State the blood parasite species.
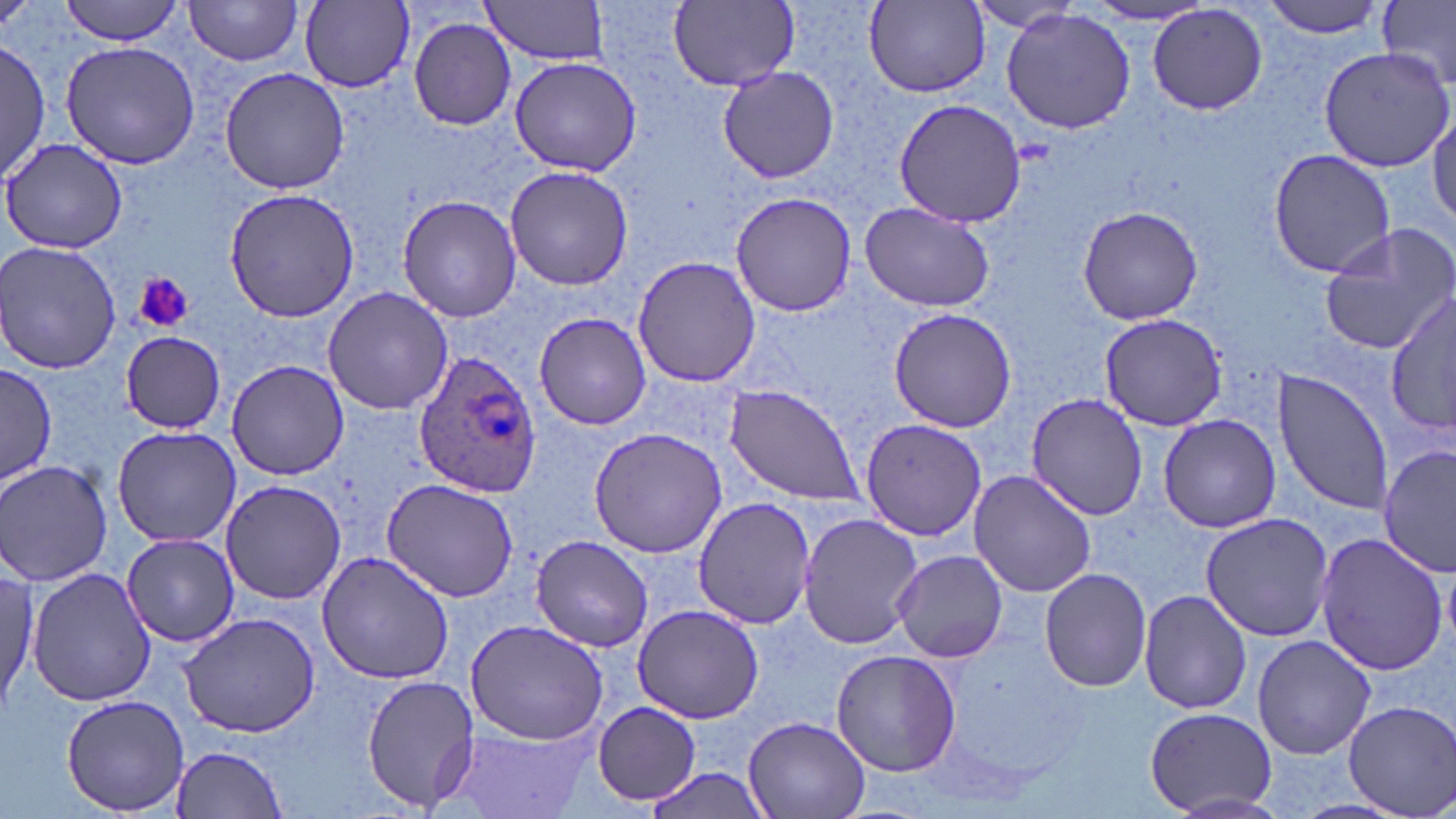

Plasmodium ovale.

Approximate bounding boxes as (x1,y1)-(x2,y2) corner pairs in pixels. Platelet locations: (136,273)-(194,333). Uninfected red blood cell locations: (62,0)-(187,45), (184,0)-(306,67), (300,0)-(417,91), (478,0)-(613,65), (1260,0)-(1392,39), (669,1)-(798,89), (865,1)-(991,97), (968,2)-(1089,33), (1377,2)-(1456,84), (1077,4)-(1212,26), (1147,4)-(1268,117), (1000,9)-(1138,135), (407,15)-(517,130), (0,39)-(50,181), (61,41)-(200,170), (1317,45)-(1456,172), (508,56)-(641,176), (219,66)-(349,194), (717,68)-(839,183), (892,98)-(1028,228), (1429,110)-(1455,226), (1,138)-(129,256), (1267,148)-(1396,278), (505,166)-(632,291), (224,188)-(364,322), (729,192)-(856,316), (397,195)-(521,322), (859,201)-(995,311), (1075,204)-(1204,325), (1317,223)-(1456,356), (0,243)-(125,373), (632,256)-(762,389), (321,286)-(453,416), (1386,292)-(1455,438), (887,308)-(1019,432), (533,313)-(653,430), (1096,313)-(1227,430), (120,331)-(226,434), (226,359)-(348,481), (0,364)-(54,486), (1273,368)-(1395,516), (723,384)-(863,503), (1026,392)-(1148,520), (1157,414)-(1283,533), (860,417)-(986,541), (111,425)-(242,548), (589,427)-(729,557), (1379,444)-(1455,577), (0,459)-(114,587), (967,469)-(1097,598), (219,479)-(346,605), (379,479)-(521,603), (691,497)-(815,629), (799,512)-(921,648), (1200,512)-(1333,643), (1313,531)-(1449,676), (121,534)-(243,647), (529,535)-(653,653), (891,548)-(1008,664), (317,551)-(454,685), (0,566)-(38,713), (1039,566)-(1153,692), (26,567)-(155,707), (1138,589)-(1251,715), (631,605)-(764,724), (178,610)-(323,738), (465,619)-(611,746), (1252,635)-(1375,760), (830,648)-(962,778), (359,672)-(481,814), (62,694)-(190,815), (1343,701)-(1456,817), (591,702)-(701,806), (1144,707)-(1275,815), (742,715)-(873,819), (443,724)-(598,817), (168,743)-(290,816). Plasmodium ovale-infected red blood cell locations: (414,349)-(540,499). Light microscopy. Image is 1456×819 pixels. Thin blood film. One field of a larger specimen. May-Grünwald-Giemsa-stained preparation. 1000x magnification.